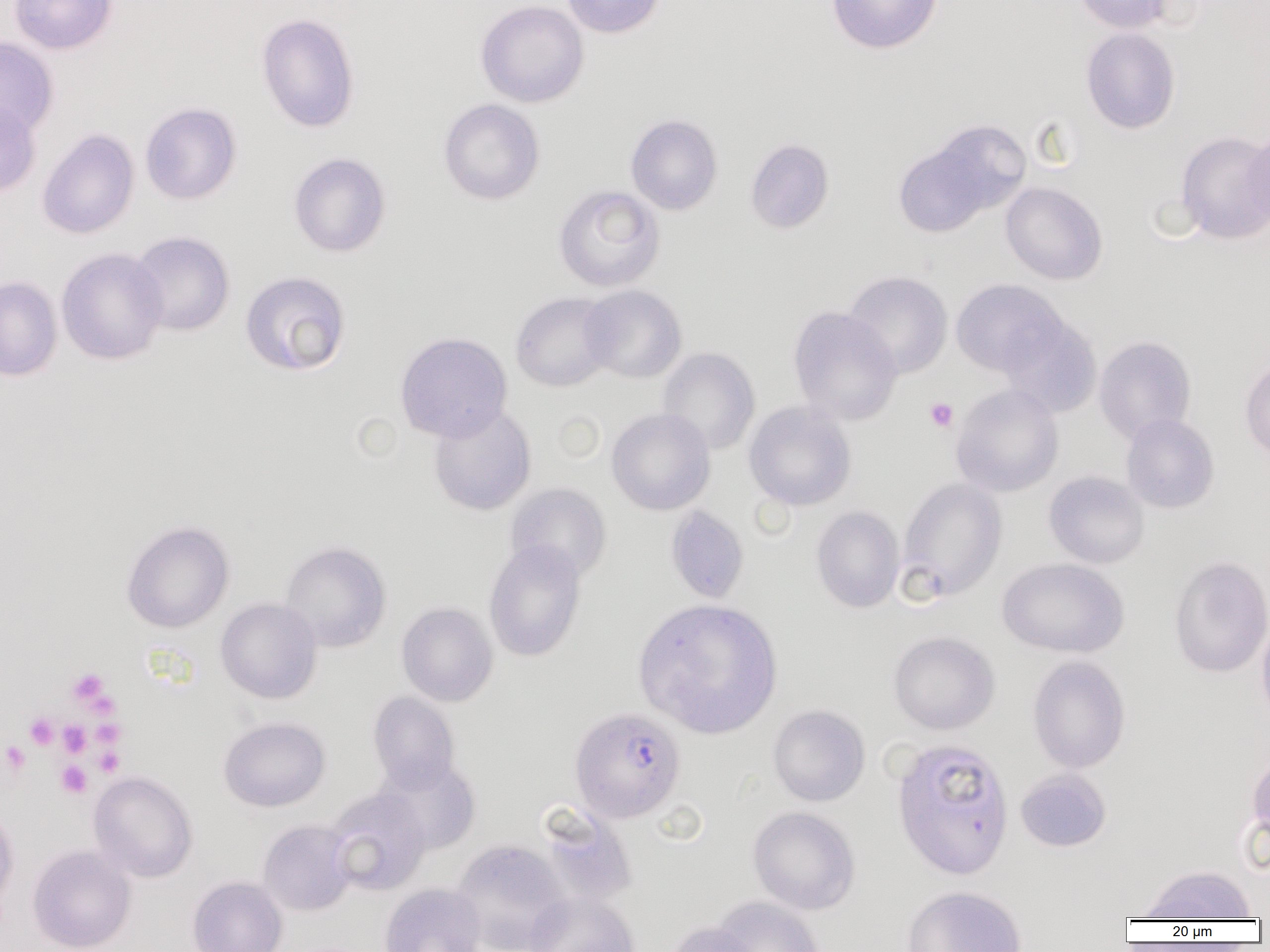
slide_level_diagnosis: Plasmodium falciparum
modality: optical microscopy
plasmodium_falciparum_infected_red_blood_cell_locations: 'approximate bounding boxes as [x1, y1, x2, y2] in pixels: [570, 706, 686, 823]'
image_size: 1270×952 pixels
uninfected_red_blood_cell_locations: 'approximate bounding boxes as [x1, y1, x2, y2] in pixels: [9, 0, 117, 54], [475, 0, 589, 108], [561, 0, 667, 38], [827, 0, 943, 55], [1074, 0, 1175, 34], [256, 13, 360, 133], [1081, 27, 1181, 134], [0, 36, 59, 140], [438, 98, 545, 205], [0, 100, 41, 198], [140, 102, 242, 205], [625, 113, 723, 216], [895, 122, 1028, 233], [1244, 126, 1270, 231], [37, 128, 139, 240], [1176, 131, 1270, 245], [744, 137, 834, 235], [288, 152, 391, 258], [1001, 182, 1108, 285], [552, 185, 665, 292], [128, 231, 235, 337], [56, 247, 168, 365], [240, 270, 351, 377], [843, 270, 953, 378], [0, 275, 62, 381], [950, 278, 1068, 377], [580, 284, 687, 384], [510, 291, 617, 392], [787, 306, 903, 425], [999, 314, 1102, 417], [394, 331, 512, 442], [1094, 336, 1197, 444], [656, 347, 760, 456], [1239, 355, 1270, 464], [951, 383, 1064, 497], [743, 400, 857, 511], [428, 403, 537, 516], [606, 407, 716, 515], [1120, 413, 1219, 514], [1043, 470, 1150, 569], [897, 477, 1007, 601], [505, 483, 612, 583], [665, 505, 749, 604], [811, 506, 905, 613], [121, 520, 234, 633], [279, 540, 391, 653], [483, 540, 586, 662], [1168, 555, 1270, 678], [997, 557, 1129, 658], [216, 597, 322, 704], [633, 598, 783, 739], [396, 602, 498, 706], [1256, 617, 1270, 727], [888, 631, 1000, 735], [1027, 655, 1131, 774], [367, 691, 460, 791], [767, 704, 870, 806], [218, 717, 330, 812], [891, 738, 1014, 880], [1246, 751, 1270, 851], [375, 757, 481, 855], [1015, 769, 1111, 852], [88, 771, 198, 883], [325, 788, 432, 896], [536, 804, 639, 908], [0, 806, 20, 908], [748, 806, 861, 915], [257, 819, 358, 917], [450, 838, 570, 952], [27, 845, 136, 952], [1135, 864, 1257, 921], [187, 876, 288, 952], [379, 882, 487, 952], [902, 885, 1027, 952], [525, 891, 639, 952], [711, 896, 825, 952], [664, 920, 764, 952]'
magnification: 1000x
preparation: thin blood smear
field_of_view: single
platelet_locations: 'approximate bounding boxes as [x1, y1, x2, y2] in pixels: [924, 397, 958, 432], [66, 668, 113, 710], [25, 713, 59, 750], [92, 719, 126, 748], [57, 720, 91, 757], [1, 741, 31, 777], [93, 746, 125, 776], [56, 761, 92, 798]'